Give the position of every Plasmodium parasite visible.
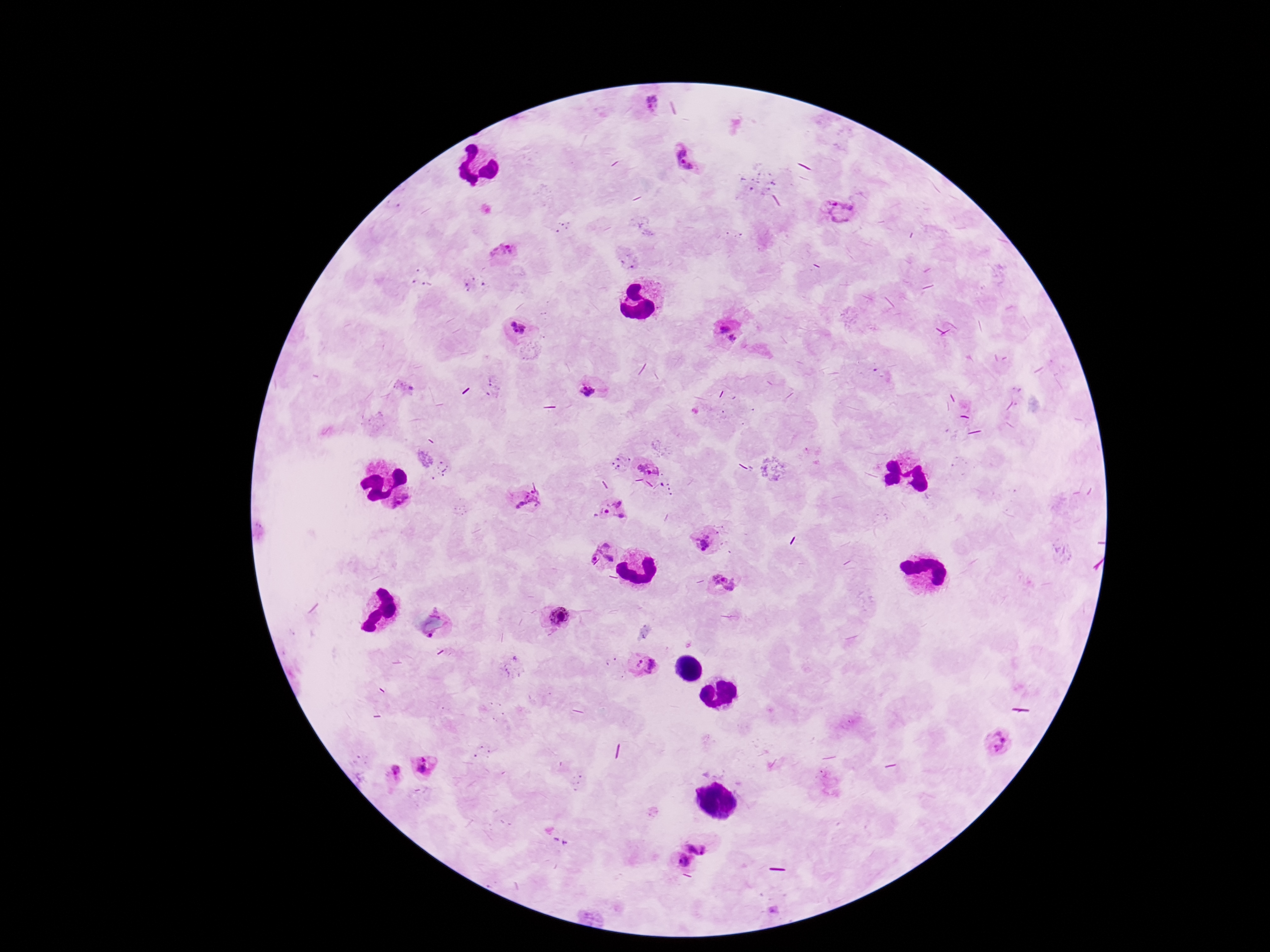

Approximate object centers, in pixels from the top-left corner.
Plasmodium parasites: (x=645, y=99), (x=687, y=163), (x=841, y=213), (x=498, y=250), (x=516, y=328), (x=730, y=332), (x=591, y=389), (x=649, y=467), (x=524, y=502), (x=613, y=511), (x=706, y=539), (x=602, y=554), (x=724, y=584), (x=558, y=618), (x=431, y=636), (x=642, y=664), (x=999, y=741), (x=423, y=767), (x=392, y=771), (x=700, y=838), (x=681, y=862).

preparation: thick peripheral-blood smear
stain: Giemsa
field_of_view: single
patient_malaria_status: infected
magnification: 100x
image_size: 1270×952 pixels
capture: smartphone camera through the microscope eyepiece